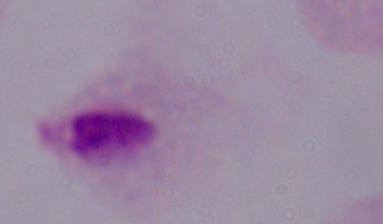
{
  "magnification": "1000x",
  "modality": "micrograph",
  "identification": "trichomonad"
}